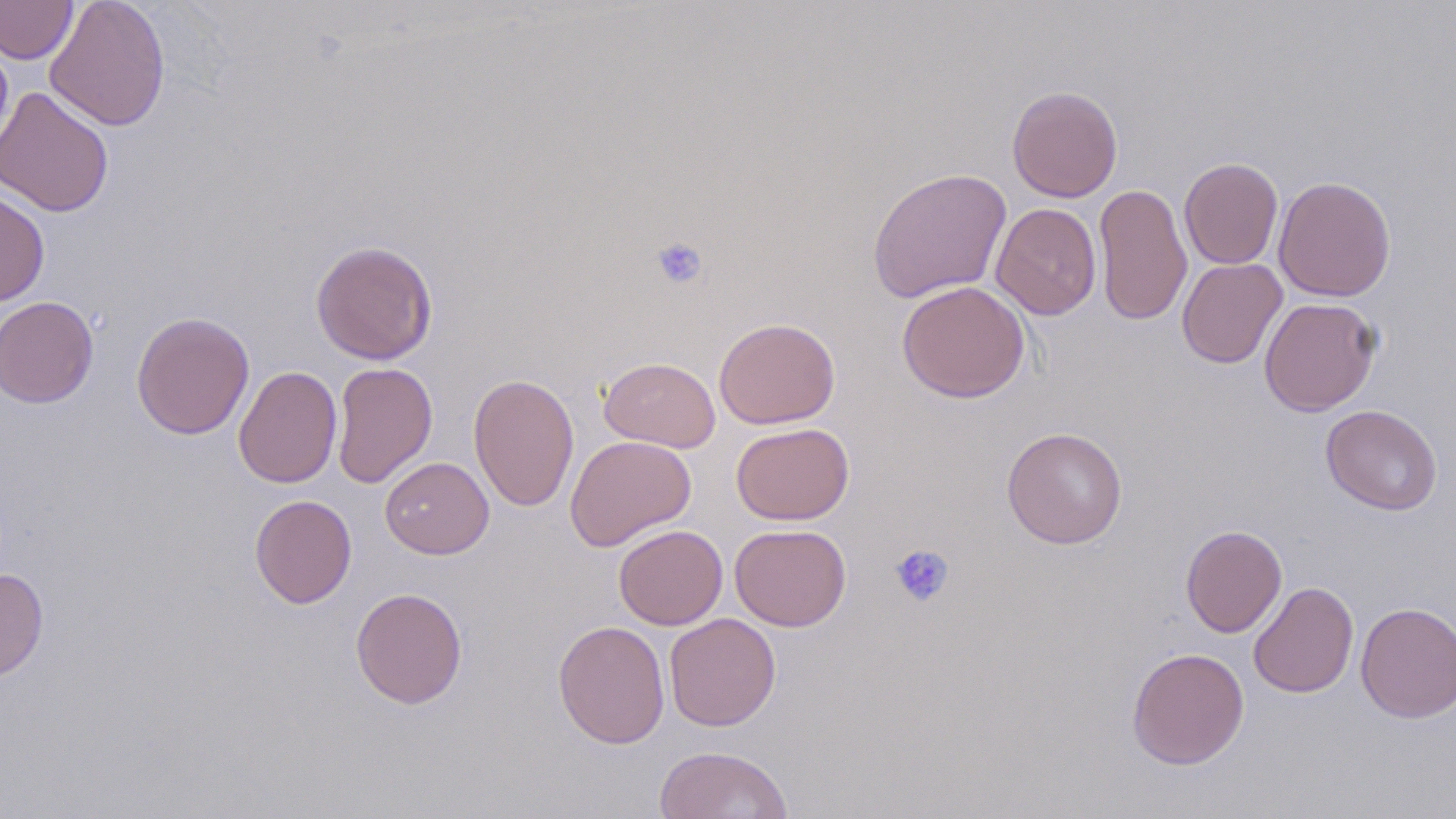 Approximate bounding boxes as [x1, y1, x2, y2] in pixels. Uninfected red blood cell locations: [0, 0, 78, 64], [45, 0, 170, 131], [0, 35, 13, 156], [0, 86, 115, 217], [1007, 86, 1122, 202], [1179, 157, 1283, 270], [867, 167, 1012, 303], [1273, 176, 1396, 301], [1093, 182, 1192, 326], [0, 187, 50, 306], [991, 203, 1102, 320], [310, 240, 438, 365], [1177, 258, 1288, 369], [896, 280, 1030, 403], [1, 296, 99, 408], [1259, 296, 1381, 416], [131, 311, 254, 439], [714, 317, 841, 429], [599, 357, 721, 452], [331, 362, 438, 489], [234, 366, 342, 489], [468, 372, 579, 512], [1321, 405, 1443, 515], [731, 422, 854, 526], [1002, 426, 1127, 548], [565, 435, 697, 551], [379, 456, 494, 559], [250, 494, 357, 609], [613, 524, 728, 630], [730, 524, 851, 631], [1180, 524, 1287, 638], [0, 568, 49, 681], [1248, 581, 1358, 698], [350, 587, 468, 708], [1355, 601, 1456, 723], [664, 613, 781, 731], [553, 620, 670, 748], [1126, 647, 1250, 770], [654, 745, 794, 819]. Platelet locations: [650, 236, 708, 290], [889, 544, 955, 608]. Slide-level diagnosis: no evidence of blood parasites. Captured at 1000x magnification. Image is 1456×819 pixels. Thin blood smear. One field of a larger specimen. May-Grünwald-Giemsa stain. Light microscopy.